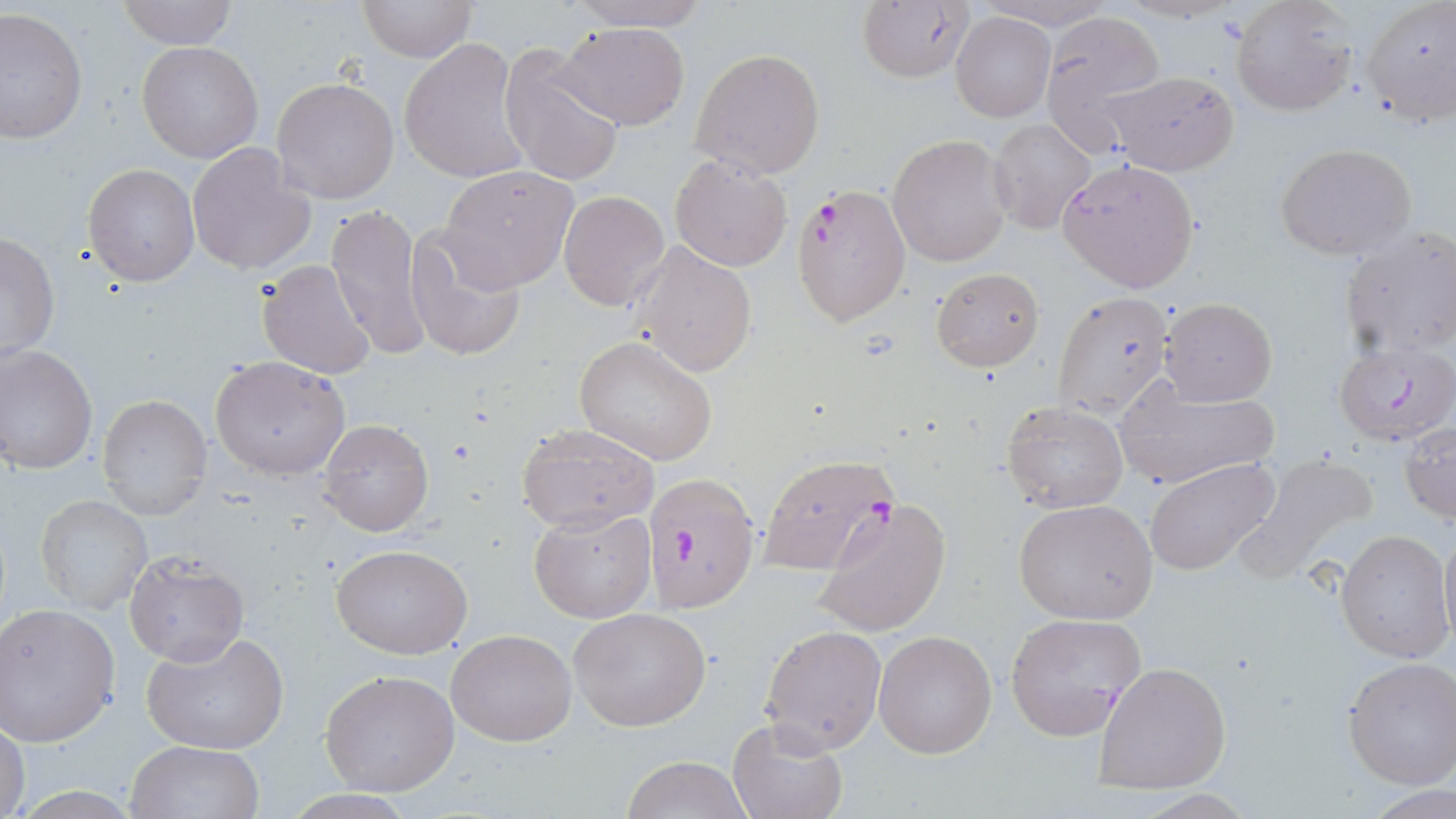
{
  "slide_level_diagnosis": "Plasmodium falciparum",
  "preparation": "thin blood film",
  "image_size": "1456×819 pixels",
  "modality": "optical microscopy",
  "field_of_view": "single",
  "magnification": "1000x",
  "plasmodium_falciparum_infected_red_blood_cell_locations": "approximate bounding boxes as (x1, y1, x2, y2) in pixels: (793, 182, 912, 326), (1332, 342, 1453, 446), (757, 455, 897, 572), (643, 471, 761, 614)",
  "stain": "May-Grünwald-Giemsa",
  "uninfected_red_blood_cell_locations": "approximate bounding boxes as (x1, y1, x2, y2) in pixels: (114, 0, 239, 49), (358, 0, 475, 61), (564, 0, 714, 31), (857, 0, 976, 84), (971, 0, 1119, 31), (1229, 1, 1355, 117), (1361, 1, 1455, 128), (1, 8, 87, 143), (1038, 10, 1165, 150), (951, 12, 1055, 122), (554, 21, 691, 131), (399, 36, 528, 184), (138, 41, 263, 163), (498, 44, 625, 188), (690, 48, 826, 178), (1100, 70, 1239, 176), (271, 77, 399, 204), (988, 119, 1096, 234), (888, 134, 1011, 266), (187, 143, 316, 276), (1275, 143, 1419, 262), (670, 154, 793, 271), (1057, 157, 1200, 292), (83, 164, 199, 285), (438, 165, 579, 293), (558, 190, 669, 310), (325, 203, 434, 362), (405, 226, 528, 362), (1339, 227, 1456, 360), (1, 231, 59, 363), (631, 242, 756, 378), (257, 258, 378, 378), (930, 267, 1045, 372), (1050, 290, 1175, 424), (1160, 297, 1278, 406), (573, 335, 719, 465), (0, 344, 98, 473), (210, 355, 350, 480), (1114, 376, 1281, 491), (97, 394, 213, 520), (1000, 400, 1129, 514), (318, 419, 433, 536), (1402, 420, 1455, 522), (517, 423, 659, 533), (1236, 453, 1384, 584), (1143, 456, 1283, 577), (35, 494, 152, 615), (1013, 497, 1160, 625), (814, 498, 953, 637), (529, 505, 655, 623), (1438, 521, 1456, 655), (1336, 529, 1451, 662), (331, 543, 474, 660), (123, 552, 248, 667), (0, 603, 122, 745), (568, 607, 712, 731), (1005, 612, 1147, 740), (759, 625, 886, 753), (448, 627, 576, 746), (141, 629, 289, 754), (874, 630, 998, 759), (1342, 656, 1456, 788), (1094, 661, 1231, 795), (319, 669, 459, 795), (1, 718, 28, 818), (727, 718, 848, 819), (125, 740, 264, 819), (622, 755, 753, 818)"
}